Name the parasite shown.
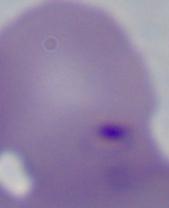

This is Babesia.

1000x magnification. Micrograph.